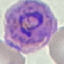
Summary:
  - Result: malaria parasites detected
  - Preparation: thin smear
  - Capture: smartphone camera at the microscope eyepiece
  - Stain: Giemsa
  - Image type: automatically extracted cell patch, resized to 64 × 64 pixels